Assess the morphology of the erythrocytes.
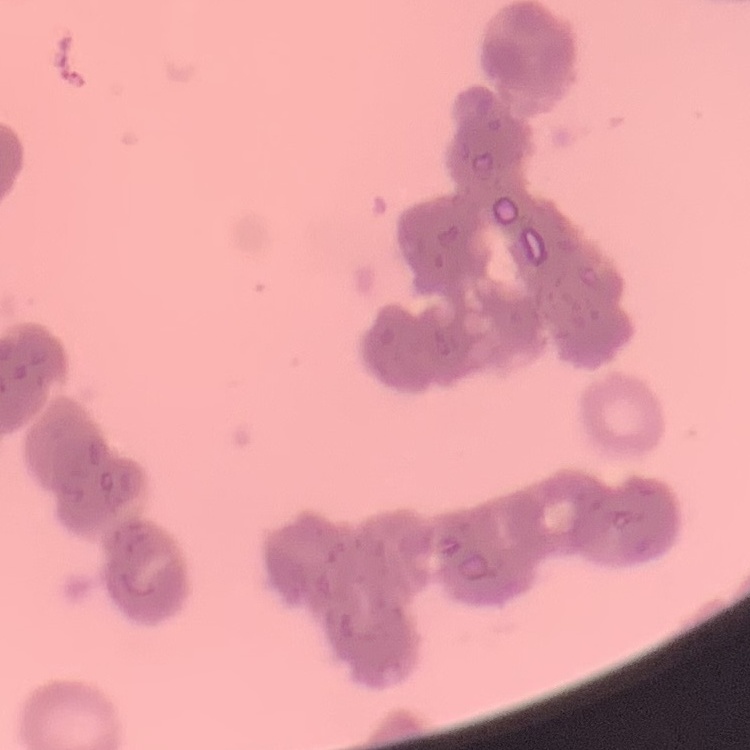
Rouleaux formation.

{
  "preparation": "thin peripheral smear",
  "stain": "Field's or Giemsa",
  "image_type": "one tile cut from a larger photomicrograph"
}